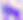

modality = micrograph
magnification = 400x
identification = Toxoplasma gondii